Comment on the morphology of the erythrocytes.
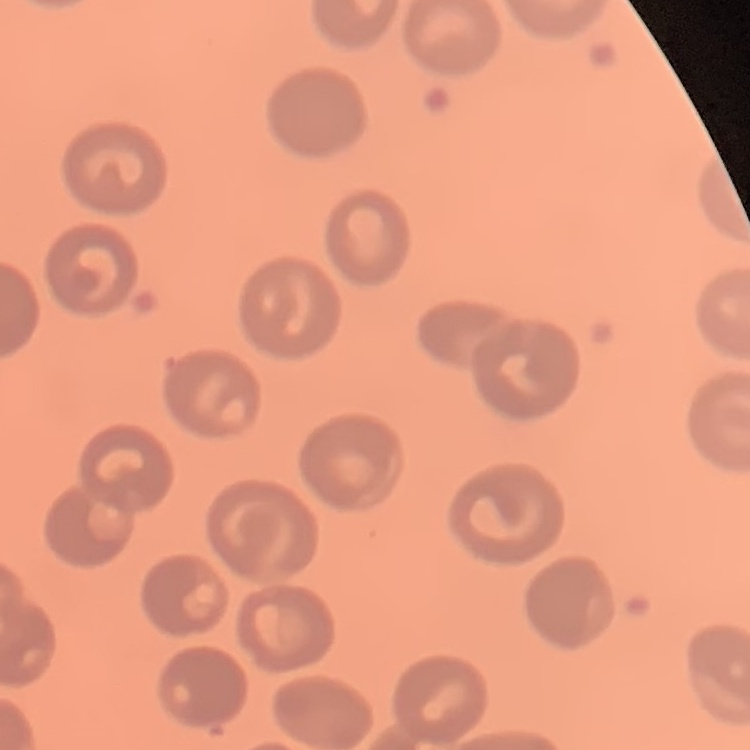
They show no rouleaux formation.

Field's or Giemsa stain. Thin blood film. Square crop of a larger photomicrograph.